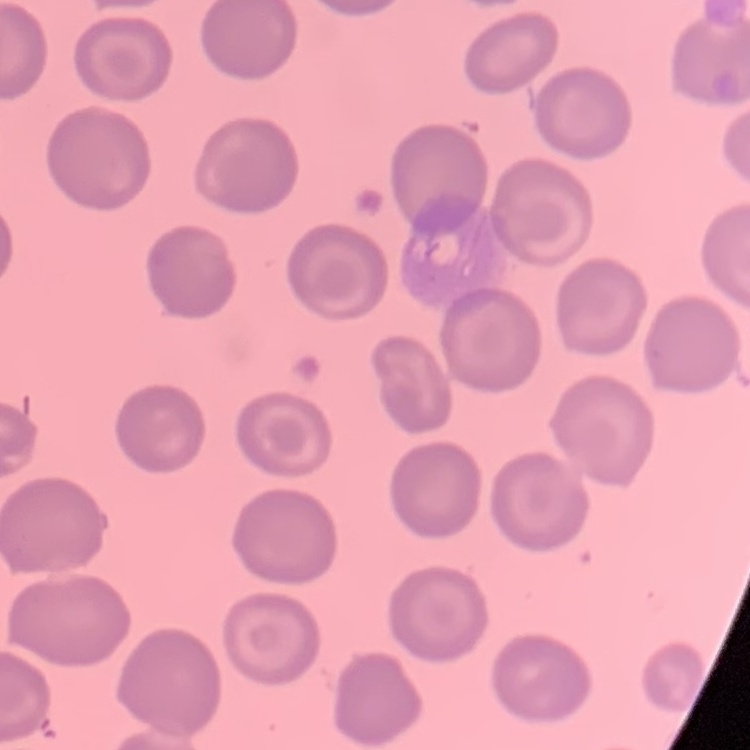

The erythrocytes show no rouleaux formation. Thin blood smear. Stained with either Field's or Giemsa. Square crop of a larger photomicrograph.